Comment on the morphology of the erythrocytes.
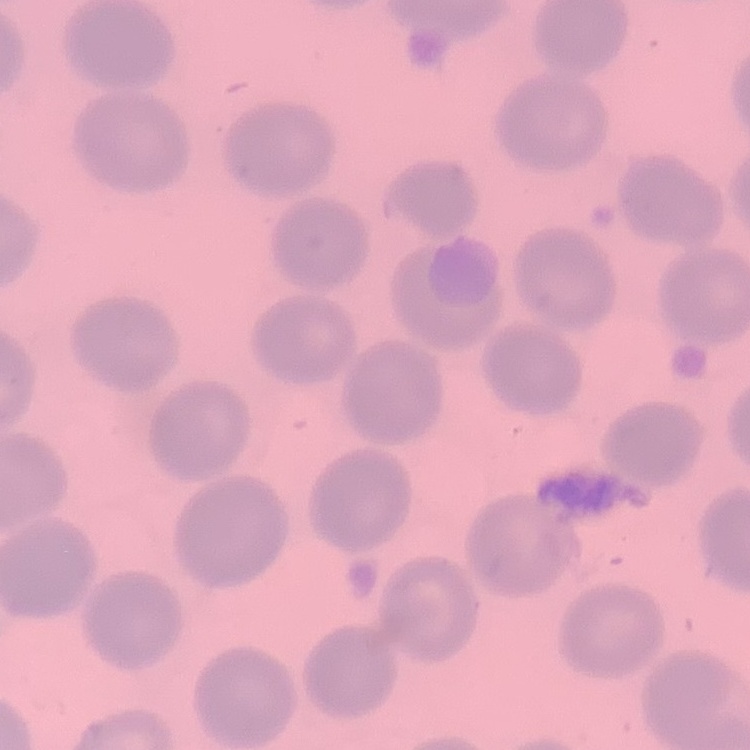

They show no rouleaux formation.

stain: Field's or Giemsa
image_type: square crop of a larger photomicrograph
preparation: thin blood smear